Name the blood parasite species.
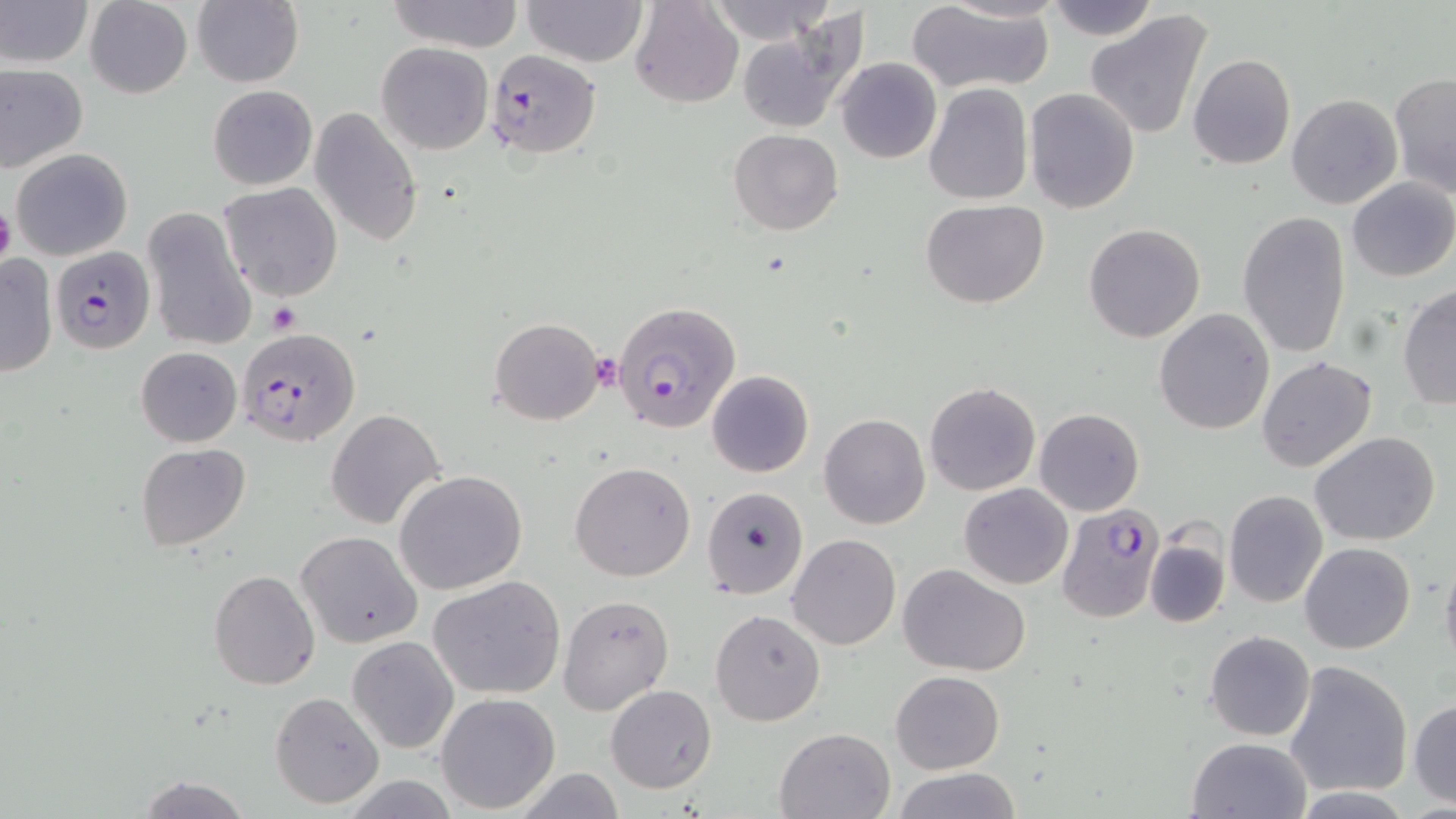

Plasmodium falciparum.

platelet locations = approximate bounding boxes as (x1, y1, x2, y2) in pixels: (0, 200, 16, 270), (268, 302, 301, 333), (587, 352, 622, 392)
stain = May-Grünwald-Giemsa
field of view = single
magnification = 1000x
modality = light microscopy
preparation = thin blood smear
Plasmodium falciparum-infected red blood cell locations = approximate bounding boxes as (x1, y1, x2, y2) in pixels: (486, 49, 598, 157), (51, 246, 156, 354), (613, 301, 741, 433), (238, 327, 360, 447), (1057, 504, 1168, 624)
image size = 1456×819 pixels
uninfected red blood cell locations = approximate bounding boxes as (x1, y1, x2, y2) in pixels: (1, 0, 92, 68), (84, 0, 193, 99), (192, 0, 304, 88), (388, 0, 522, 51), (522, 0, 648, 66), (629, 0, 743, 108), (1040, 0, 1162, 42), (705, 1, 837, 47), (905, 2, 1053, 92), (1086, 8, 1216, 141), (736, 26, 858, 133), (376, 42, 494, 155), (1188, 54, 1296, 171), (835, 57, 941, 164), (0, 62, 88, 173), (1390, 72, 1456, 198), (922, 82, 1033, 206), (207, 85, 318, 190), (1024, 87, 1140, 213), (1285, 94, 1402, 210), (309, 107, 424, 247), (728, 128, 843, 236), (11, 148, 132, 261), (1347, 176, 1456, 282), (219, 182, 344, 301), (922, 200, 1050, 310), (141, 207, 256, 354), (1236, 211, 1352, 359), (1083, 223, 1206, 343), (0, 253, 58, 378), (1398, 285, 1455, 410), (1153, 308, 1276, 434), (488, 318, 604, 425), (135, 346, 242, 446), (1255, 355, 1378, 473), (707, 371, 814, 478), (923, 383, 1042, 497), (1033, 407, 1144, 515), (327, 408, 446, 531), (820, 413, 931, 530), (1309, 431, 1441, 546), (135, 443, 250, 551), (569, 462, 696, 583), (394, 470, 529, 595), (958, 482, 1073, 589), (700, 486, 808, 599), (1224, 490, 1329, 609), (295, 529, 423, 648), (787, 534, 901, 652), (1145, 539, 1229, 628), (1299, 542, 1416, 655), (1439, 546, 1456, 672), (900, 564, 1031, 677), (208, 571, 321, 691), (429, 576, 567, 700), (557, 593, 675, 717), (710, 609, 825, 726), (1204, 630, 1314, 741), (347, 636, 460, 754), (1283, 660, 1413, 798), (890, 670, 1004, 774), (606, 685, 716, 794), (270, 691, 385, 810), (436, 692, 561, 812), (1409, 698, 1456, 806), (773, 727, 895, 819), (1185, 737, 1313, 819), (890, 768, 1021, 819), (509, 770, 630, 818), (136, 774, 253, 818)